Name the parasite shown.
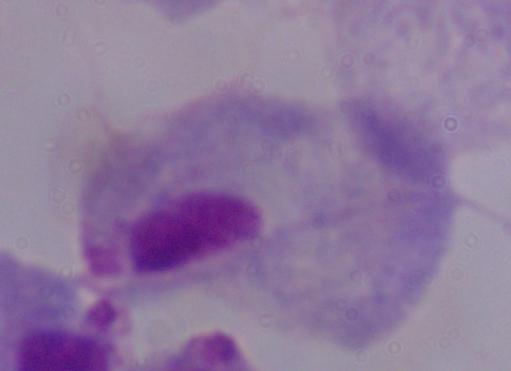
A trichomonad.

magnification = 1000x
modality = photomicrograph